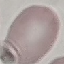

result = no malaria parasites detected
image type = automatically extracted cell patch, resized to 64 × 64 pixels
stain = Giemsa
capture = smartphone through the microscope eyepiece
preparation = thin blood film